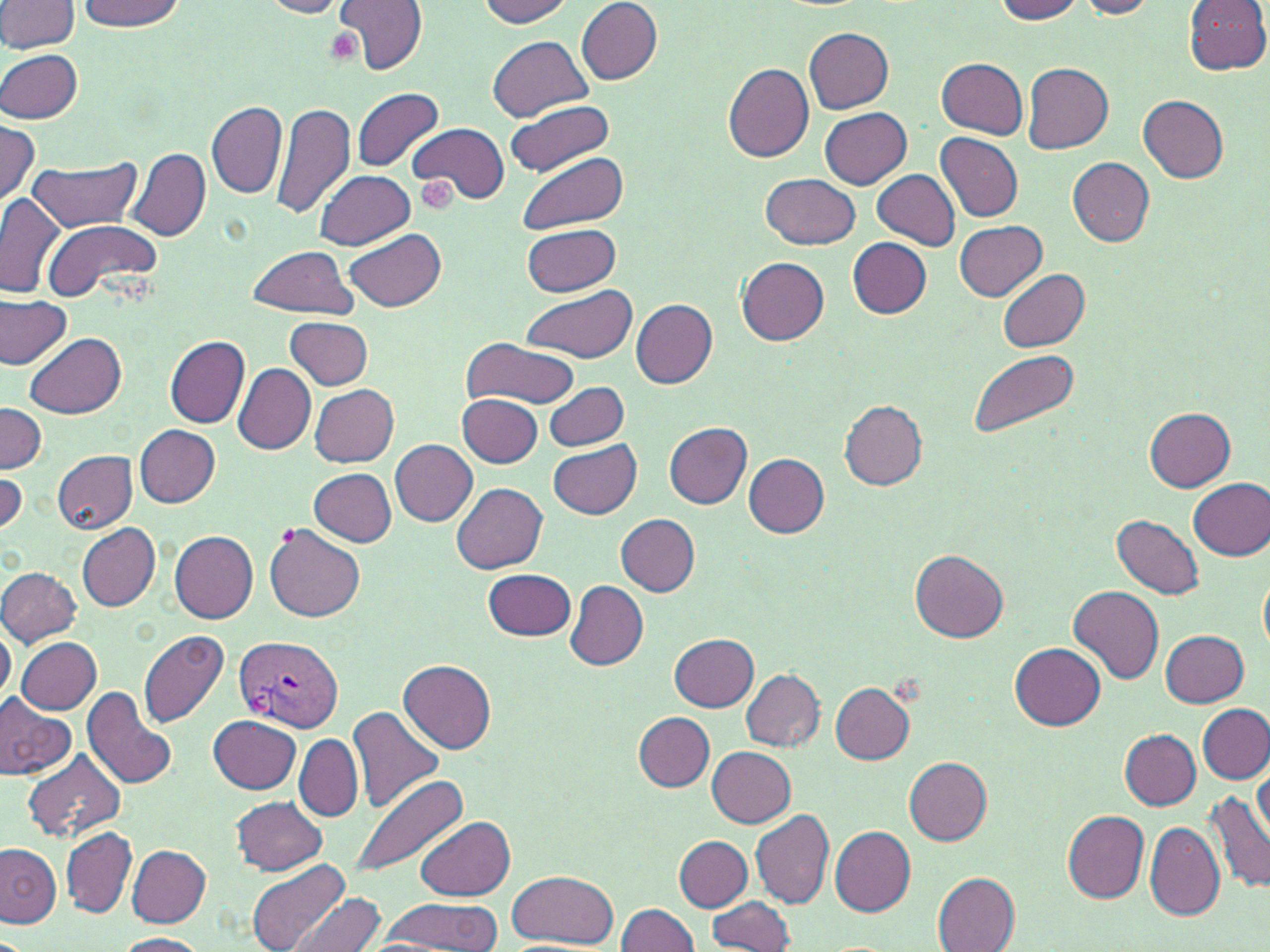
{
  "plasmodium_vivax_infected_red_blood_cell_locations": "approximate bounding boxes as [x1, y1, x2, y2] in pixels: [235, 634, 343, 734]",
  "slide_level_diagnosis": "Plasmodium vivax",
  "modality": "optical microscopy",
  "stain": "May-Grünwald-Giemsa",
  "uninfected_red_blood_cell_locations": "approximate bounding boxes as [x1, y1, x2, y2] in pixels: [259, 0, 353, 18], [334, 0, 427, 76], [477, 0, 575, 26], [992, 0, 1087, 23], [1075, 0, 1160, 18], [1183, 0, 1270, 75], [0, 1, 80, 54], [75, 1, 187, 31], [576, 2, 661, 85], [804, 28, 893, 112], [487, 35, 593, 120], [0, 47, 84, 123], [938, 58, 1027, 137], [1023, 62, 1113, 152], [723, 63, 814, 163], [353, 88, 445, 171], [1137, 94, 1229, 183], [504, 98, 618, 176], [207, 101, 287, 199], [270, 102, 358, 219], [820, 107, 912, 189], [0, 121, 40, 208], [407, 123, 507, 205], [936, 134, 1023, 222], [126, 147, 210, 242], [516, 153, 629, 234], [28, 157, 142, 232], [1067, 157, 1155, 245], [872, 168, 960, 250], [314, 169, 415, 250], [762, 173, 861, 249], [0, 193, 66, 298], [41, 218, 160, 301], [956, 221, 1047, 300], [521, 223, 621, 295], [345, 228, 447, 312], [847, 237, 931, 319], [246, 245, 358, 318], [736, 255, 829, 345], [996, 268, 1089, 352], [520, 288, 638, 363], [0, 293, 72, 369], [630, 299, 717, 388], [284, 317, 373, 389], [26, 332, 126, 418], [165, 336, 249, 427], [460, 337, 580, 410], [162, 348, 312, 444], [968, 350, 1081, 440], [234, 363, 316, 453], [543, 382, 627, 450], [309, 383, 399, 467], [458, 393, 542, 468], [840, 401, 927, 490], [0, 402, 47, 472], [1145, 407, 1235, 492], [665, 422, 752, 508], [135, 424, 221, 507], [391, 439, 478, 526], [547, 443, 642, 518], [54, 451, 138, 534], [64, 452, 148, 609], [744, 454, 830, 537], [0, 468, 24, 536], [309, 468, 397, 546], [1187, 479, 1270, 560], [453, 482, 548, 574], [615, 513, 700, 596], [1112, 514, 1204, 599], [77, 524, 161, 611], [266, 524, 365, 621], [170, 530, 258, 623], [911, 550, 1007, 642], [0, 566, 82, 646], [484, 567, 576, 641], [1258, 568, 1270, 655], [565, 581, 649, 671], [1068, 586, 1164, 686], [0, 617, 15, 705], [139, 630, 230, 726], [1162, 630, 1248, 706], [669, 633, 760, 711], [17, 637, 103, 713], [1012, 644, 1105, 730], [398, 660, 496, 753], [741, 669, 823, 752], [829, 683, 915, 763], [85, 688, 181, 789], [0, 696, 76, 782], [1198, 703, 1269, 783], [347, 706, 446, 813], [633, 712, 714, 792], [208, 716, 299, 794], [1120, 729, 1200, 810], [293, 734, 362, 822], [708, 746, 796, 827], [21, 749, 126, 845], [905, 756, 993, 845], [1253, 768, 1269, 844], [351, 772, 470, 879], [1206, 790, 1270, 895], [232, 796, 326, 874], [751, 808, 835, 909], [1063, 810, 1149, 901], [415, 816, 516, 900], [1144, 820, 1224, 921], [61, 825, 136, 918], [830, 826, 915, 916], [675, 836, 751, 911], [0, 843, 62, 926], [127, 844, 211, 926], [246, 859, 351, 952], [507, 871, 619, 949], [932, 872, 1022, 951], [292, 891, 387, 952], [707, 895, 797, 951], [376, 896, 502, 949], [615, 902, 700, 952], [113, 933, 207, 952]",
  "image_size": "1270×952 pixels",
  "platelet_locations": "approximate bounding boxes as [x1, y1, x2, y2] in pixels: [414, 176, 458, 215]",
  "preparation": "thin blood film",
  "magnification": "1000x",
  "field_of_view": "one of a larger specimen"
}